Outline each blood parasite and name the species.
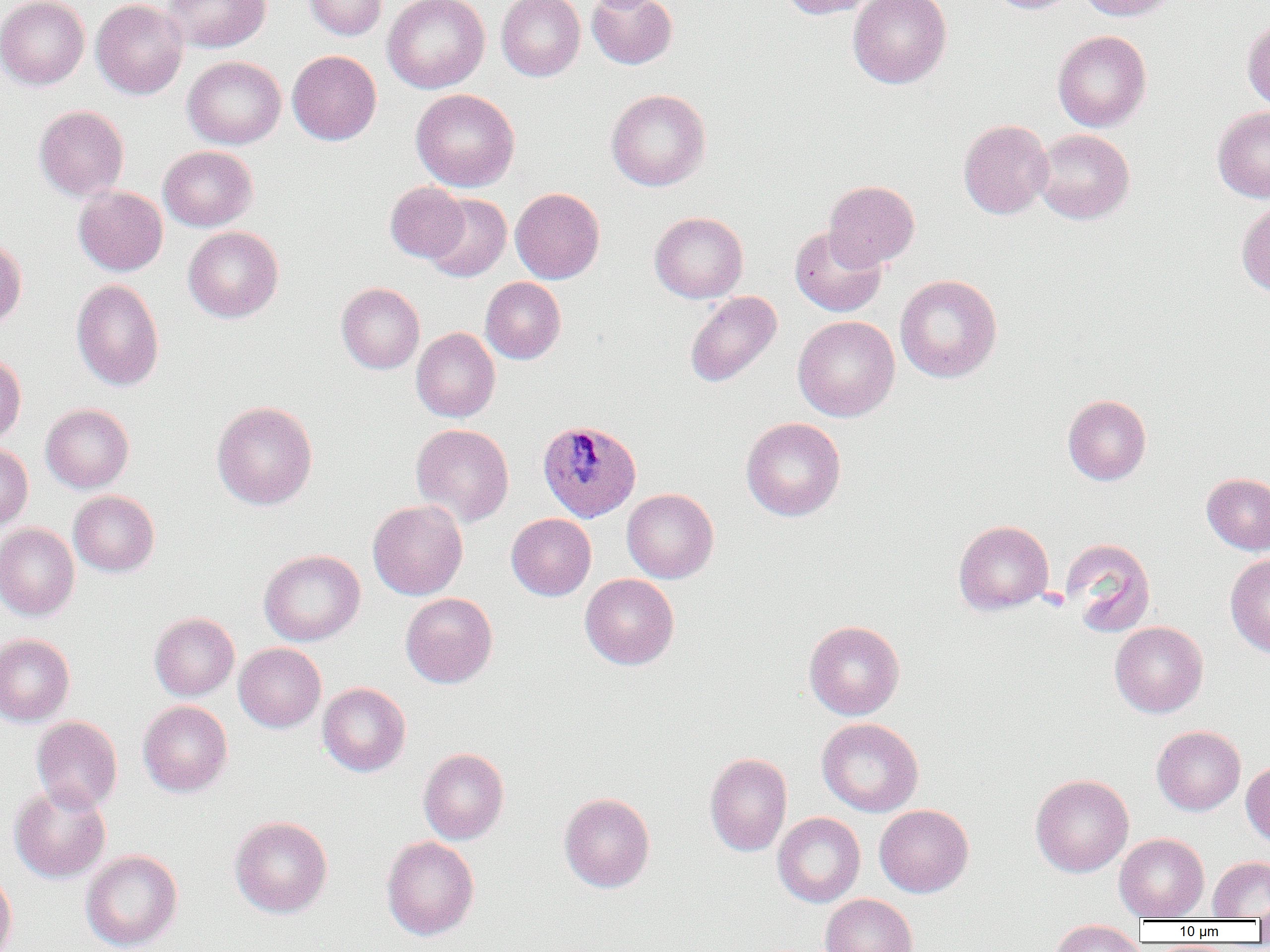
Approximate bounding boxes as (x1,y1)-(x2,y2) corner pairs in pixels.
Plasmodium ovale-infected red blood cells: (537,419)-(641,521).
No Plasmodium falciparum, Plasmodium malariae, Plasmodium vivax, Babesia divergens, or Trypanosoma brucei observed.

Uninfected red blood cell locations: (0,0)-(89,90), (91,0)-(188,99), (163,0)-(271,53), (304,0)-(388,40), (383,0)-(489,93), (496,0)-(585,81), (781,0)-(877,18), (849,0)-(952,88), (988,0)-(1080,14), (1077,0)-(1177,21), (586,1)-(677,69), (1242,17)-(1270,111), (1053,30)-(1151,132), (287,50)-(381,145), (182,56)-(286,149), (411,88)-(519,192), (606,89)-(711,191), (34,105)-(129,201), (1212,107)-(1270,203), (958,119)-(1053,219), (1033,129)-(1135,224), (158,146)-(258,231), (824,180)-(920,270), (385,182)-(469,262), (73,186)-(168,276), (511,187)-(605,283), (423,193)-(511,282), (1237,200)-(1270,297), (649,211)-(748,303), (183,226)-(283,322), (789,226)-(887,316), (0,237)-(27,330), (895,274)-(1002,383), (480,277)-(566,364), (71,279)-(164,391), (337,283)-(424,373), (684,291)-(783,388), (793,315)-(900,421), (411,327)-(500,422), (0,353)-(26,444), (1063,394)-(1151,485), (212,401)-(318,510), (40,404)-(134,492), (741,417)-(846,521), (411,423)-(515,526), (0,443)-(33,531), (1202,473)-(1270,554), (622,488)-(719,583), (69,490)-(159,577), (368,499)-(468,600), (506,513)-(596,600), (953,519)-(1054,615), (0,523)-(79,621), (1060,537)-(1155,637), (259,549)-(365,646), (1225,553)-(1270,657), (580,574)-(679,669), (400,593)-(498,688), (149,612)-(239,700), (804,620)-(905,719), (1110,621)-(1208,717), (0,634)-(75,725), (234,643)-(326,732), (318,682)-(411,777), (138,700)-(232,797), (31,716)-(123,813), (817,718)-(923,816), (1152,725)-(1245,815), (418,748)-(509,844), (705,752)-(792,856), (1241,759)-(1270,847), (1030,774)-(1134,877), (9,783)-(111,883), (559,792)-(655,892), (874,804)-(973,897), (773,813)-(865,907), (230,816)-(333,917), (1114,833)-(1209,921), (381,836)-(480,940), (81,849)-(182,952), (1208,856)-(1270,919), (0,868)-(17,952), (820,894)-(917,952), (1255,895)-(1270,930), (1049,920)-(1146,952). Platelet locations: (1038,587)-(1070,612). Slide-level diagnosis: Plasmodium ovale. Optical microscopy. Image is 1270×952 pixels. Single field of view. Thin blood film. 1000x magnification.